Assess this cell for malaria.
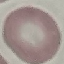
Uninfected.

Giemsa-stained preparation. Automatically extracted cell patch, resized to 64 × 64 pixels. Acquired by smartphone through the microscope eyepiece. Thin blood film.